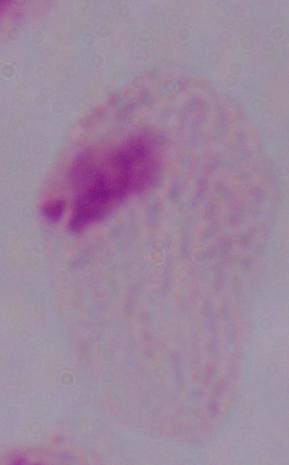
Summary:
  - Magnification: 1000x
  - Identification: trichomonad
  - Modality: micrograph